Locate every Plasmodium parasite.
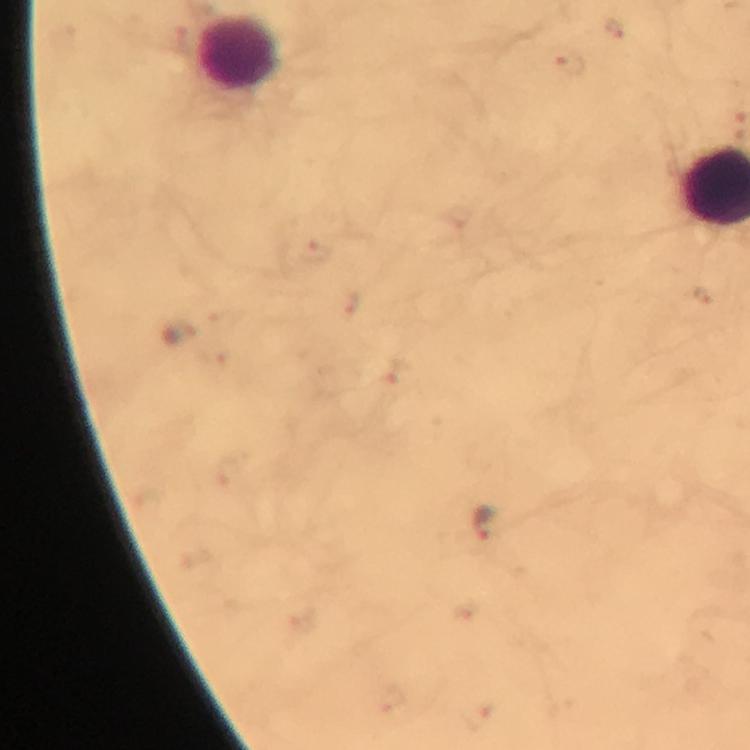

Approximate object centers, in pixels from the top-left corner.
Plasmodium parasites: (x=569, y=63), (x=316, y=252), (x=704, y=293), (x=346, y=303), (x=179, y=333), (x=397, y=374), (x=485, y=522).

preparation = thick smear
magnification = 100x
capture = smartphone photograph through a microscope
immersion oil = applied
context = from a malaria diagnostic workup
stain = Giemsa
leukocyte locations = approximate object centers, in pixels from the top-left corner: (x=240, y=56)
cropped from = a single field of view
image size = 750×750 pixels